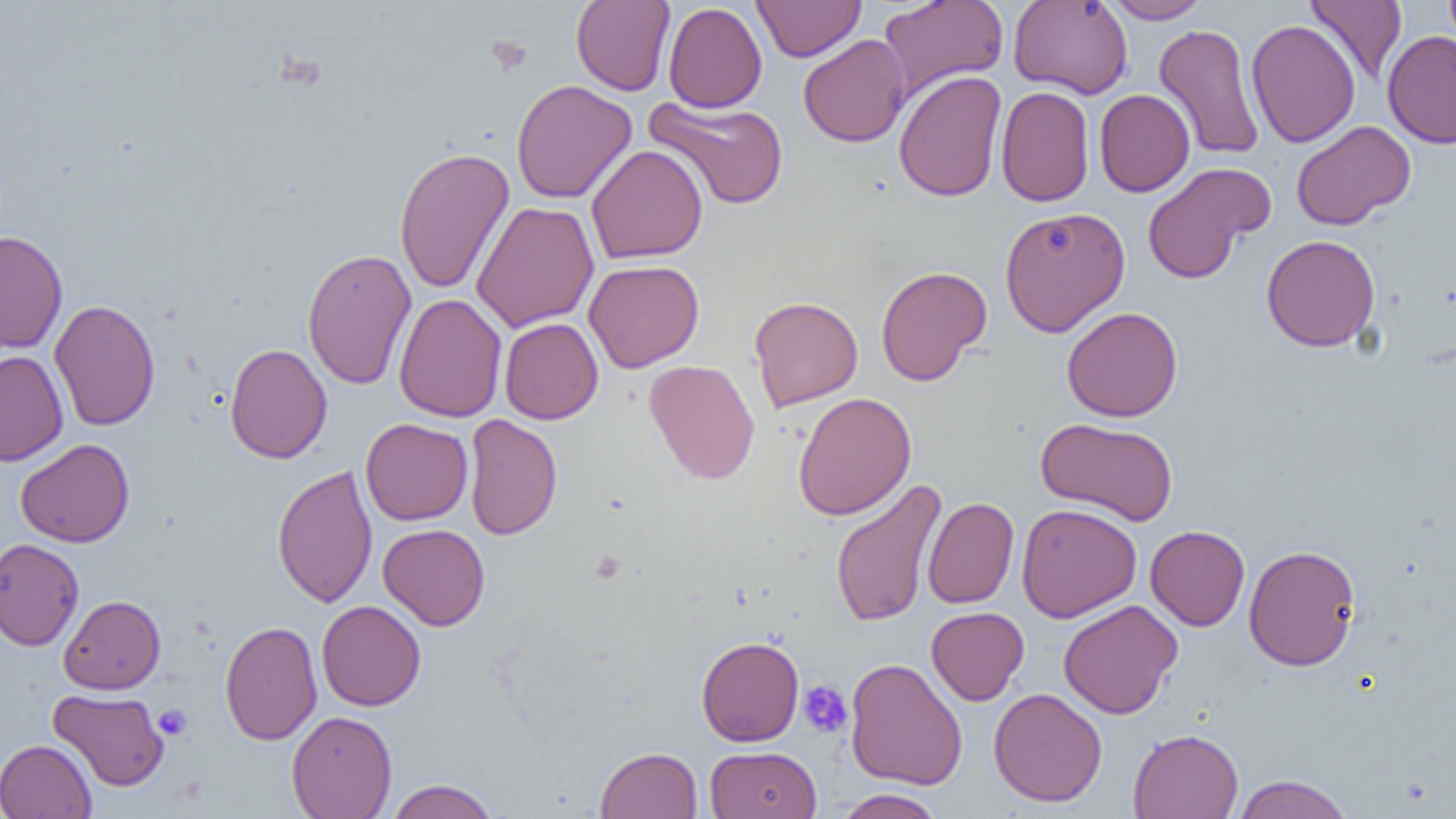
slide_level_diagnosis: no evidence of blood parasites
modality: optical microscopy
preparation: thin blood film
image_size: 1456×819 pixels
magnification: 1000x
uninfected_red_blood_cell_locations: 'approximate bounding boxes as named x1/y1/x2/y2 corners in pixels: (x1=571, y1=0, x2=676, y2=96), (x1=753, y1=0, x2=865, y2=62), (x1=877, y1=0, x2=1009, y2=101), (x1=1009, y1=0, x2=1133, y2=99), (x1=1101, y1=0, x2=1211, y2=23), (x1=1306, y1=0, x2=1407, y2=86), (x1=1443, y1=0, x2=1456, y2=51), (x1=663, y1=2, x2=767, y2=113), (x1=1245, y1=19, x2=1360, y2=148), (x1=1153, y1=23, x2=1265, y2=161), (x1=1383, y1=29, x2=1456, y2=149), (x1=798, y1=34, x2=911, y2=147), (x1=894, y1=70, x2=1007, y2=202), (x1=511, y1=78, x2=637, y2=204), (x1=995, y1=86, x2=1095, y2=207), (x1=1094, y1=89, x2=1195, y2=197), (x1=644, y1=96, x2=790, y2=211), (x1=1290, y1=120, x2=1416, y2=231), (x1=586, y1=144, x2=708, y2=264), (x1=393, y1=146, x2=514, y2=295), (x1=1142, y1=162, x2=1275, y2=284), (x1=471, y1=201, x2=599, y2=333), (x1=999, y1=206, x2=1130, y2=336), (x1=0, y1=231, x2=68, y2=354), (x1=1261, y1=234, x2=1380, y2=352), (x1=302, y1=248, x2=416, y2=390), (x1=583, y1=260, x2=704, y2=373), (x1=876, y1=265, x2=991, y2=386), (x1=393, y1=293, x2=507, y2=423), (x1=749, y1=295, x2=863, y2=411), (x1=49, y1=299, x2=160, y2=431), (x1=1062, y1=306, x2=1183, y2=422), (x1=499, y1=318, x2=603, y2=424), (x1=224, y1=343, x2=332, y2=463), (x1=0, y1=350, x2=68, y2=466), (x1=644, y1=359, x2=760, y2=485), (x1=793, y1=392, x2=916, y2=520), (x1=463, y1=414, x2=562, y2=540), (x1=1035, y1=417, x2=1178, y2=526), (x1=360, y1=418, x2=473, y2=525), (x1=15, y1=438, x2=135, y2=547), (x1=272, y1=462, x2=378, y2=608), (x1=829, y1=476, x2=945, y2=629), (x1=923, y1=497, x2=1018, y2=608), (x1=1016, y1=502, x2=1141, y2=623), (x1=378, y1=524, x2=490, y2=630), (x1=1145, y1=525, x2=1250, y2=631), (x1=0, y1=538, x2=84, y2=651), (x1=1243, y1=544, x2=1361, y2=671), (x1=59, y1=594, x2=166, y2=694), (x1=1058, y1=599, x2=1182, y2=719), (x1=317, y1=600, x2=426, y2=711), (x1=926, y1=607, x2=1028, y2=705), (x1=220, y1=620, x2=322, y2=745), (x1=696, y1=636, x2=804, y2=746), (x1=845, y1=658, x2=967, y2=790), (x1=988, y1=687, x2=1107, y2=807), (x1=48, y1=689, x2=169, y2=791), (x1=286, y1=710, x2=397, y2=819), (x1=1128, y1=728, x2=1244, y2=819), (x1=0, y1=739, x2=97, y2=819), (x1=705, y1=745, x2=822, y2=818), (x1=596, y1=746, x2=702, y2=818), (x1=1231, y1=774, x2=1355, y2=818), (x1=385, y1=779, x2=499, y2=819), (x1=835, y1=789, x2=946, y2=819)'
field_of_view: one of a larger specimen
platelet_locations: 'approximate bounding boxes as named x1/y1/x2/y2 corners in pixels: (x1=485, y1=35, x2=532, y2=76), (x1=798, y1=681, x2=852, y2=738), (x1=153, y1=704, x2=193, y2=740)'